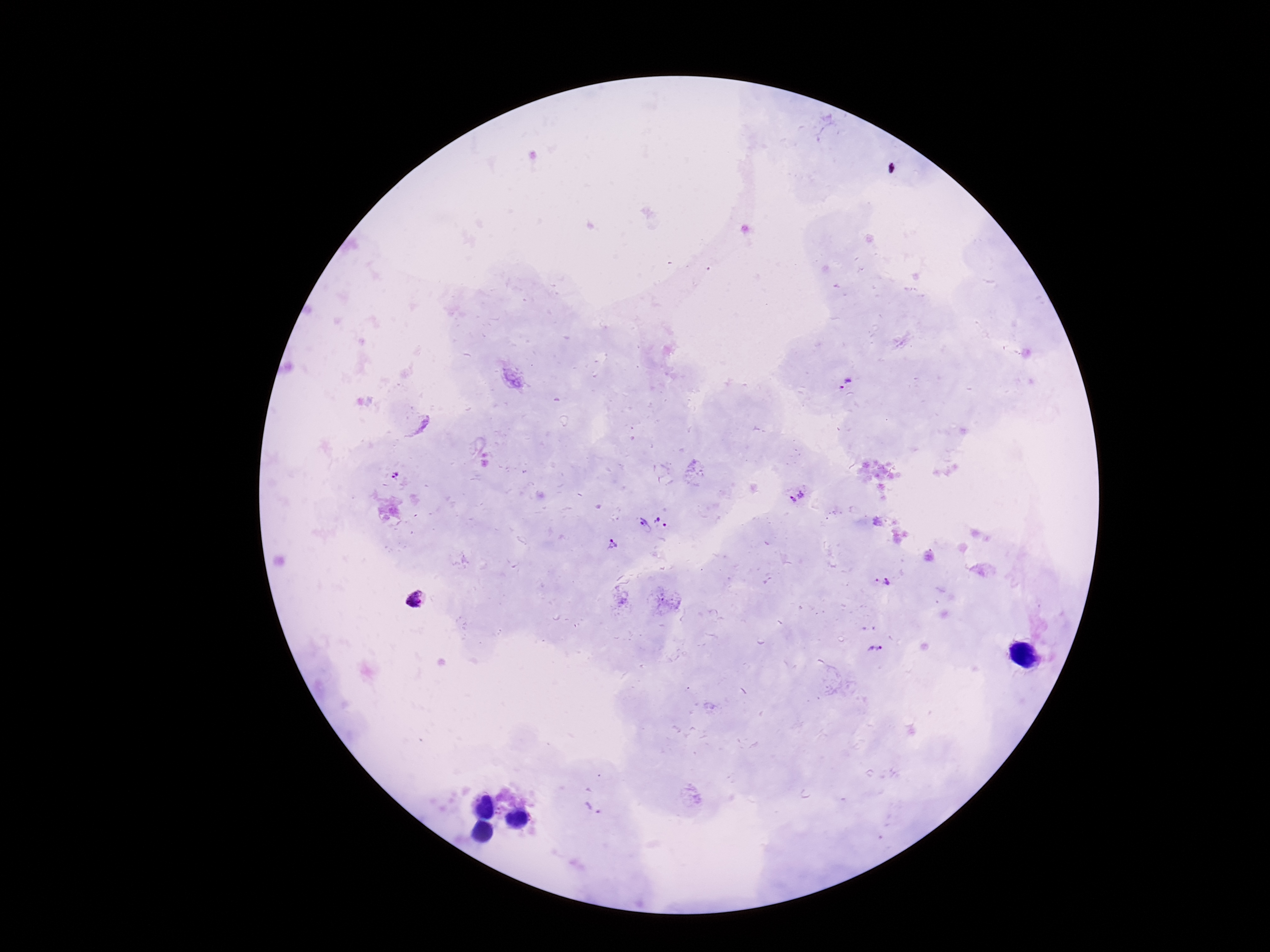
Approximate centers as (x, y) in pixels.
Summary:
  - Plasmodium parasite locations: (847, 383), (395, 474), (796, 494), (662, 521), (642, 526), (613, 545), (875, 581), (888, 582), (416, 601), (875, 649), (806, 793), (592, 808)
  - Image size: 1270×952 pixels
  - Magnification: 100x
  - Field of view: single
  - Capture: smartphone camera through the microscope eyepiece
  - Stain: Giemsa
  - Patient malaria status: positive
  - Preparation: thick peripheral-blood smear